Report the malaria status of this cell.
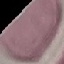
It is uninfected.

Cell patch, automatically extracted from a larger field of view and resized to 64 × 64 pixels. Thin blood smear. Giemsa stain. Photographed with a smartphone camera at the microscope eyepiece.